Assess this cell for malaria.
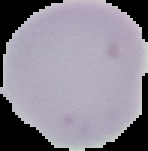
Uninfected.

image type = segmented cell region with the area outside set to black
image size = 148×151 pixels
preparation = thin blood film